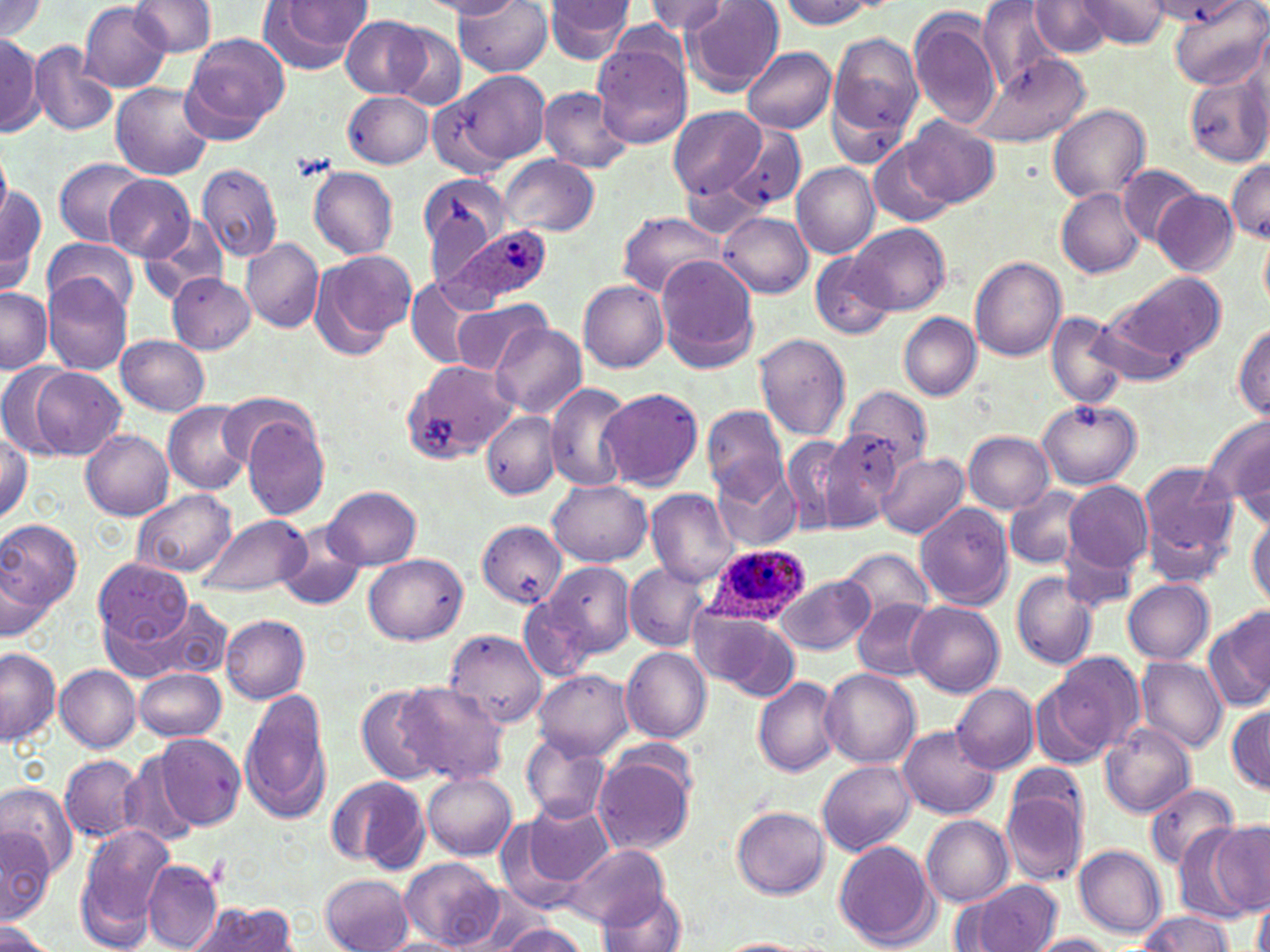
Summary:
  - Coordinate format: approximate bounding boxes as named x1/y1/x2/y2 corners in pixels
  - Plasmodium ovale-infected red blood cell locations: (x1=441, y1=223, x2=555, y2=307), (x1=703, y1=543, x2=810, y2=626)
  - Platelet locations: (x1=293, y1=152, x2=334, y2=181)
  - Uninfected red blood cell locations: (x1=422, y1=0, x2=523, y2=18), (x1=543, y1=0, x2=637, y2=66), (x1=682, y1=0, x2=785, y2=94), (x1=976, y1=0, x2=1064, y2=94), (x1=1076, y1=0, x2=1175, y2=49), (x1=1167, y1=0, x2=1267, y2=89), (x1=0, y1=1, x2=48, y2=43), (x1=129, y1=1, x2=217, y2=57), (x1=644, y1=1, x2=727, y2=35), (x1=779, y1=1, x2=881, y2=29), (x1=79, y1=2, x2=172, y2=91), (x1=258, y1=2, x2=373, y2=74), (x1=456, y1=2, x2=553, y2=77), (x1=1029, y1=2, x2=1113, y2=57), (x1=909, y1=10, x2=1004, y2=129), (x1=342, y1=16, x2=429, y2=97), (x1=388, y1=25, x2=469, y2=110), (x1=827, y1=29, x2=925, y2=157), (x1=181, y1=33, x2=289, y2=143), (x1=0, y1=34, x2=42, y2=136), (x1=591, y1=41, x2=693, y2=150), (x1=28, y1=43, x2=117, y2=136), (x1=741, y1=47, x2=836, y2=134), (x1=971, y1=55, x2=1089, y2=149), (x1=424, y1=70, x2=548, y2=166), (x1=1183, y1=74, x2=1270, y2=167), (x1=110, y1=83, x2=214, y2=180), (x1=538, y1=85, x2=636, y2=173), (x1=342, y1=91, x2=434, y2=168), (x1=1048, y1=105, x2=1152, y2=204), (x1=668, y1=106, x2=765, y2=199), (x1=901, y1=115, x2=1000, y2=207), (x1=728, y1=124, x2=806, y2=212), (x1=868, y1=143, x2=953, y2=227), (x1=0, y1=148, x2=11, y2=224), (x1=498, y1=154, x2=598, y2=238), (x1=55, y1=158, x2=150, y2=246), (x1=1227, y1=158, x2=1270, y2=241), (x1=791, y1=162, x2=879, y2=258), (x1=195, y1=163, x2=283, y2=262), (x1=1119, y1=164, x2=1202, y2=245), (x1=308, y1=166, x2=398, y2=259), (x1=418, y1=173, x2=510, y2=272), (x1=679, y1=173, x2=772, y2=239), (x1=106, y1=175, x2=195, y2=261), (x1=0, y1=180, x2=47, y2=295), (x1=1057, y1=187, x2=1145, y2=278), (x1=1154, y1=189, x2=1239, y2=275), (x1=617, y1=211, x2=724, y2=297), (x1=719, y1=212, x2=813, y2=297), (x1=140, y1=214, x2=229, y2=303), (x1=848, y1=223, x2=950, y2=315), (x1=1259, y1=232, x2=1270, y2=312), (x1=43, y1=236, x2=138, y2=317), (x1=242, y1=238, x2=323, y2=333), (x1=310, y1=249, x2=417, y2=357), (x1=810, y1=251, x2=896, y2=341), (x1=654, y1=256, x2=758, y2=373), (x1=971, y1=257, x2=1066, y2=362), (x1=1111, y1=271, x2=1227, y2=364), (x1=167, y1=272, x2=256, y2=354), (x1=45, y1=277, x2=131, y2=375), (x1=406, y1=277, x2=483, y2=369), (x1=579, y1=281, x2=669, y2=372), (x1=0, y1=286, x2=51, y2=373), (x1=450, y1=299, x2=553, y2=376), (x1=1093, y1=302, x2=1202, y2=388), (x1=898, y1=312, x2=982, y2=401), (x1=1046, y1=312, x2=1132, y2=408), (x1=490, y1=322, x2=587, y2=420), (x1=1233, y1=322, x2=1270, y2=419), (x1=116, y1=334, x2=211, y2=416), (x1=755, y1=334, x2=851, y2=441), (x1=402, y1=359, x2=512, y2=463), (x1=0, y1=363, x2=78, y2=457), (x1=23, y1=367, x2=127, y2=460), (x1=545, y1=383, x2=632, y2=493), (x1=842, y1=385, x2=931, y2=474), (x1=597, y1=387, x2=704, y2=491), (x1=1037, y1=398, x2=1142, y2=488), (x1=164, y1=402, x2=252, y2=494), (x1=703, y1=406, x2=788, y2=501), (x1=482, y1=411, x2=559, y2=499), (x1=240, y1=413, x2=333, y2=521), (x1=1207, y1=415, x2=1270, y2=520), (x1=0, y1=428, x2=32, y2=524), (x1=80, y1=429, x2=174, y2=520), (x1=819, y1=431, x2=902, y2=528), (x1=962, y1=431, x2=1054, y2=513), (x1=777, y1=433, x2=863, y2=536), (x1=878, y1=451, x2=969, y2=539), (x1=1138, y1=461, x2=1240, y2=583), (x1=717, y1=465, x2=801, y2=550), (x1=545, y1=479, x2=652, y2=565), (x1=1062, y1=481, x2=1153, y2=573), (x1=324, y1=486, x2=422, y2=569), (x1=1005, y1=486, x2=1089, y2=571), (x1=646, y1=489, x2=739, y2=588), (x1=132, y1=490, x2=237, y2=576), (x1=916, y1=503, x2=1013, y2=609), (x1=1247, y1=512, x2=1270, y2=609), (x1=197, y1=513, x2=310, y2=596), (x1=0, y1=519, x2=83, y2=610), (x1=477, y1=521, x2=566, y2=608), (x1=274, y1=524, x2=370, y2=613), (x1=1062, y1=541, x2=1138, y2=616), (x1=840, y1=548, x2=935, y2=628), (x1=364, y1=553, x2=468, y2=645), (x1=0, y1=559, x2=56, y2=640), (x1=94, y1=560, x2=193, y2=647), (x1=543, y1=561, x2=636, y2=658), (x1=623, y1=563, x2=711, y2=651), (x1=1011, y1=572, x2=1100, y2=671), (x1=775, y1=573, x2=874, y2=654), (x1=1123, y1=578, x2=1214, y2=665), (x1=117, y1=596, x2=230, y2=684), (x1=518, y1=597, x2=598, y2=682), (x1=854, y1=600, x2=939, y2=679), (x1=907, y1=601, x2=1005, y2=696), (x1=689, y1=606, x2=801, y2=701), (x1=1206, y1=608, x2=1270, y2=714), (x1=221, y1=615, x2=311, y2=703), (x1=443, y1=630, x2=547, y2=726), (x1=0, y1=646, x2=60, y2=745), (x1=620, y1=647, x2=712, y2=743), (x1=1048, y1=653, x2=1144, y2=757), (x1=1135, y1=656, x2=1228, y2=754), (x1=55, y1=665, x2=142, y2=752), (x1=134, y1=668, x2=227, y2=741), (x1=819, y1=668, x2=920, y2=770), (x1=534, y1=670, x2=633, y2=758), (x1=754, y1=676, x2=843, y2=776), (x1=392, y1=680, x2=509, y2=785), (x1=952, y1=683, x2=1038, y2=774), (x1=1031, y1=683, x2=1112, y2=771), (x1=355, y1=684, x2=451, y2=785), (x1=238, y1=686, x2=335, y2=826), (x1=1227, y1=702, x2=1269, y2=794), (x1=899, y1=725, x2=998, y2=818), (x1=1100, y1=725, x2=1196, y2=818), (x1=522, y1=732, x2=610, y2=823), (x1=155, y1=733, x2=245, y2=829), (x1=60, y1=754, x2=144, y2=844), (x1=118, y1=754, x2=200, y2=847), (x1=593, y1=755, x2=693, y2=856), (x1=818, y1=762, x2=916, y2=855), (x1=999, y1=767, x2=1093, y2=887), (x1=423, y1=772, x2=517, y2=860), (x1=325, y1=775, x2=427, y2=870), (x1=1, y1=782, x2=79, y2=880), (x1=1145, y1=783, x2=1240, y2=870), (x1=511, y1=800, x2=614, y2=899), (x1=732, y1=806, x2=831, y2=898), (x1=920, y1=815, x2=1014, y2=906), (x1=1186, y1=820, x2=1267, y2=923), (x1=75, y1=822, x2=175, y2=947), (x1=1, y1=825, x2=55, y2=923), (x1=833, y1=840, x2=938, y2=950), (x1=565, y1=844, x2=669, y2=928), (x1=1074, y1=846, x2=1166, y2=938), (x1=400, y1=856, x2=504, y2=951), (x1=143, y1=859, x2=222, y2=952), (x1=320, y1=874, x2=415, y2=952), (x1=966, y1=879, x2=1062, y2=952), (x1=595, y1=889, x2=688, y2=952), (x1=1252, y1=900, x2=1270, y2=952), (x1=189, y1=903, x2=298, y2=952), (x1=1137, y1=912, x2=1232, y2=952), (x1=492, y1=921, x2=591, y2=951), (x1=0, y1=922, x2=57, y2=952), (x1=1025, y1=934, x2=1120, y2=952), (x1=380, y1=937, x2=472, y2=952), (x1=716, y1=938, x2=811, y2=952)
  - Slide-level diagnosis: Plasmodium ovale
  - Image size: 1270×952 pixels
  - Field of view: one of a larger specimen
  - Preparation: thin blood film
  - Magnification: 1000x
  - Modality: light microscopy
  - Stain: May-Grünwald-Giemsa